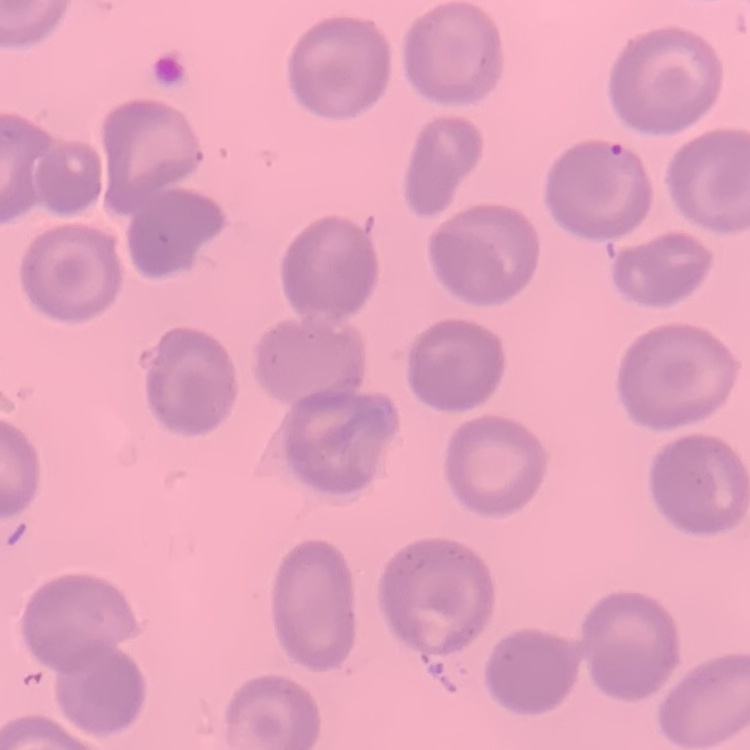
erythrocyte morphology = no rouleaux formation
image type = one tile cut from a larger photomicrograph
stain = Field's or Giemsa
preparation = thin blood smear